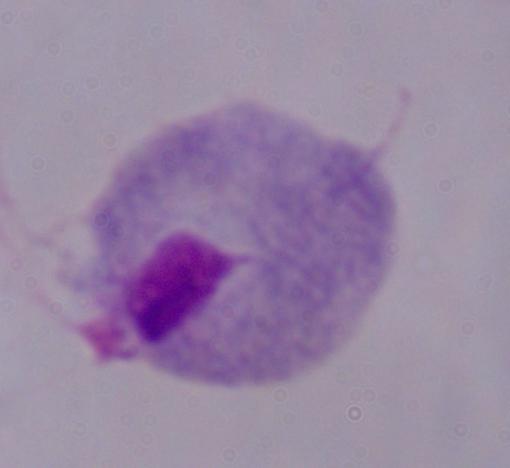

Summary:
  - Magnification: 1000x
  - Modality: photomicrograph
  - Identification: trichomonad